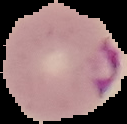
From a thin blood smear. Image is 127×124 pixels. Cell region segmented out of the field of view; the surrounding area is masked to black. Malaria status: parasitized.